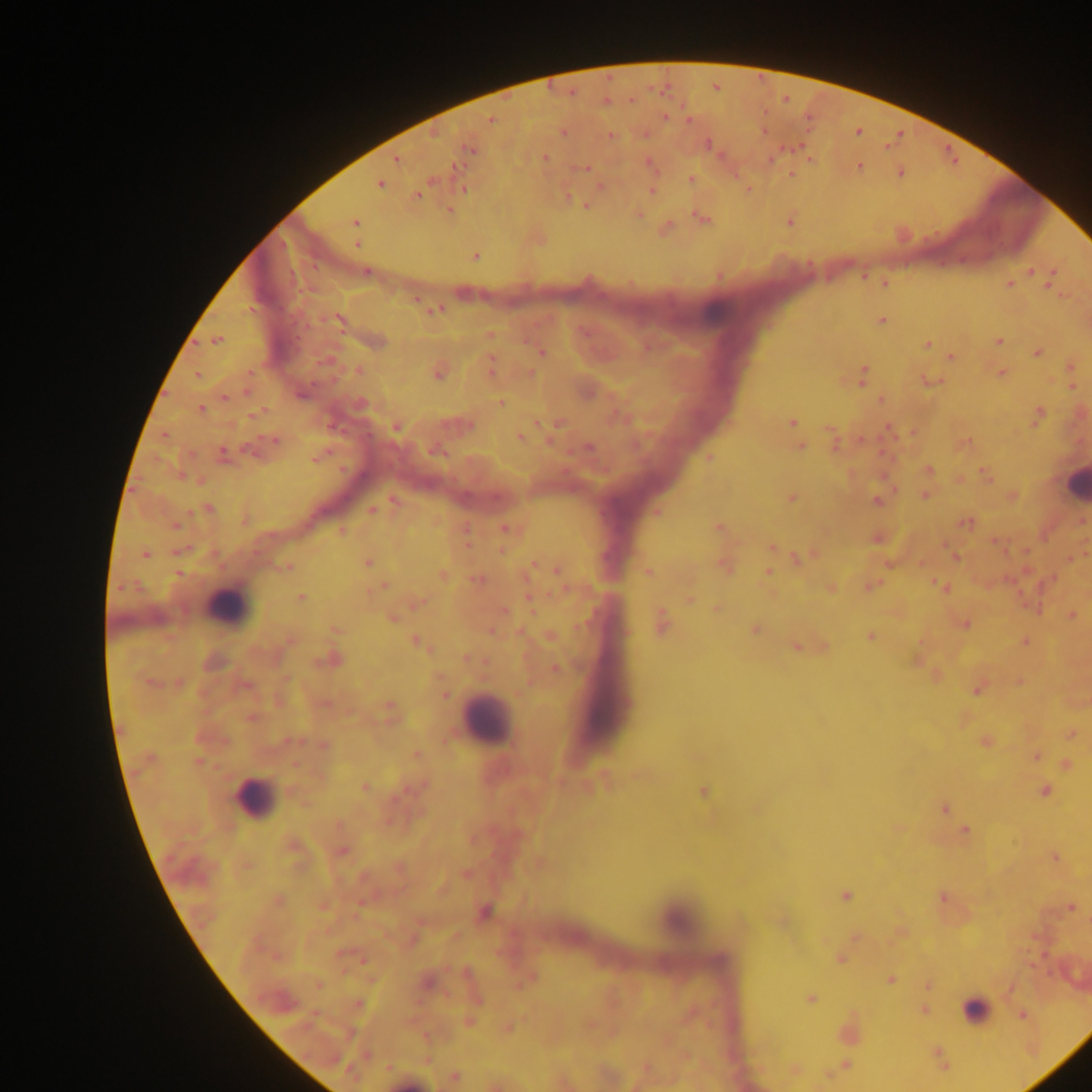

Approximate centers as x y in pixels.
Summary:
  - Malaria parasite locations: 606 101; 664 117; 490 120; 688 120; 858 131; 562 132; 609 135; 707 144; 470 148; 544 157; 396 158; 650 166; 860 166; 585 169; 900 172; 791 174; 691 179; 379 183; 600 186; 463 189; 652 189; 747 189; 417 194; 586 205; 449 210; 638 213; 701 218; 788 220; 354 222; 665 227; 357 244; 474 255; 1030 271; 366 272; 863 276; 1051 277; 885 283; 1009 283; 1063 294; 416 299; 435 309; 340 320; 882 320; 489 334; 216 340; 376 341; 998 342; 927 344; 541 352; 1037 353; 952 357; 1070 366; 491 368; 358 370; 438 371; 1001 372; 529 373; 197 375; 864 375; 1071 375; 932 380; 1072 386; 247 389; 224 397; 881 400; 501 402; 359 404; 200 409; 256 413; 1038 414; 791 422; 558 423; 459 424; 396 427; 887 429; 913 432; 831 433; 519 437; 274 440; 860 440; 963 443; 800 447; 588 448; 436 449; 222 454; 318 456; 710 457; 927 470; 985 474; 959 480; 894 490; 924 494; 1011 496; 791 497; 877 500; 394 501; 208 509; 371 510; 655 512; 965 522; 175 525; 717 527; 506 528; 342 530; 877 537; 465 541; 995 541; 772 547; 179 551; 777 551; 145 554; 807 555; 954 557; 1069 558; 797 559; 367 563; 890 563; 921 564; 530 565; 724 565; 287 566; 557 570; 647 571; 767 572; 443 576; 476 579; 384 586; 871 586; 941 587; 830 588; 300 598; 689 599; 417 602; 716 608; 503 611; 1071 615; 391 617; 661 622; 964 624; 334 628; 755 630; 491 631; 550 636; 870 636; 288 641; 1025 641; 416 642; 797 646; 468 658; 331 660; 916 660; 554 668; 1019 681; 178 684; 979 687; 444 695; 324 703; 389 709; 251 717; 1070 734; 291 741; 985 741; 324 745; 416 755; 1036 756; 1066 764; 637 775; 364 787; 1044 791; 704 792; 944 808; 898 828; 965 830; 292 847; 341 851; 1055 857; 539 863; 465 874; 845 895; 942 896; 277 901; 322 905; 1070 907; 484 913; 855 937; 361 958; 840 958; 529 978; 890 979; 426 981; 928 986; 811 999; 358 1004; 924 1009; 690 1013; 1022 1015; 468 1021; 590 1024; 507 1027; 847 1031; 366 1055; 938 1055; 846 1063; 645 1068; 793 1069; 454 1076; 494 1084
  - Leukocyte locations: 1076 484; 226 606; 487 720; 254 798; 675 920; 976 1010; 408 1082
  - Capture: mobile-phone photograph through a microscope
  - Country: Ghana
  - Image size: 1092×1092 pixels
  - Field of view: single
  - Preparation: thick blood smear